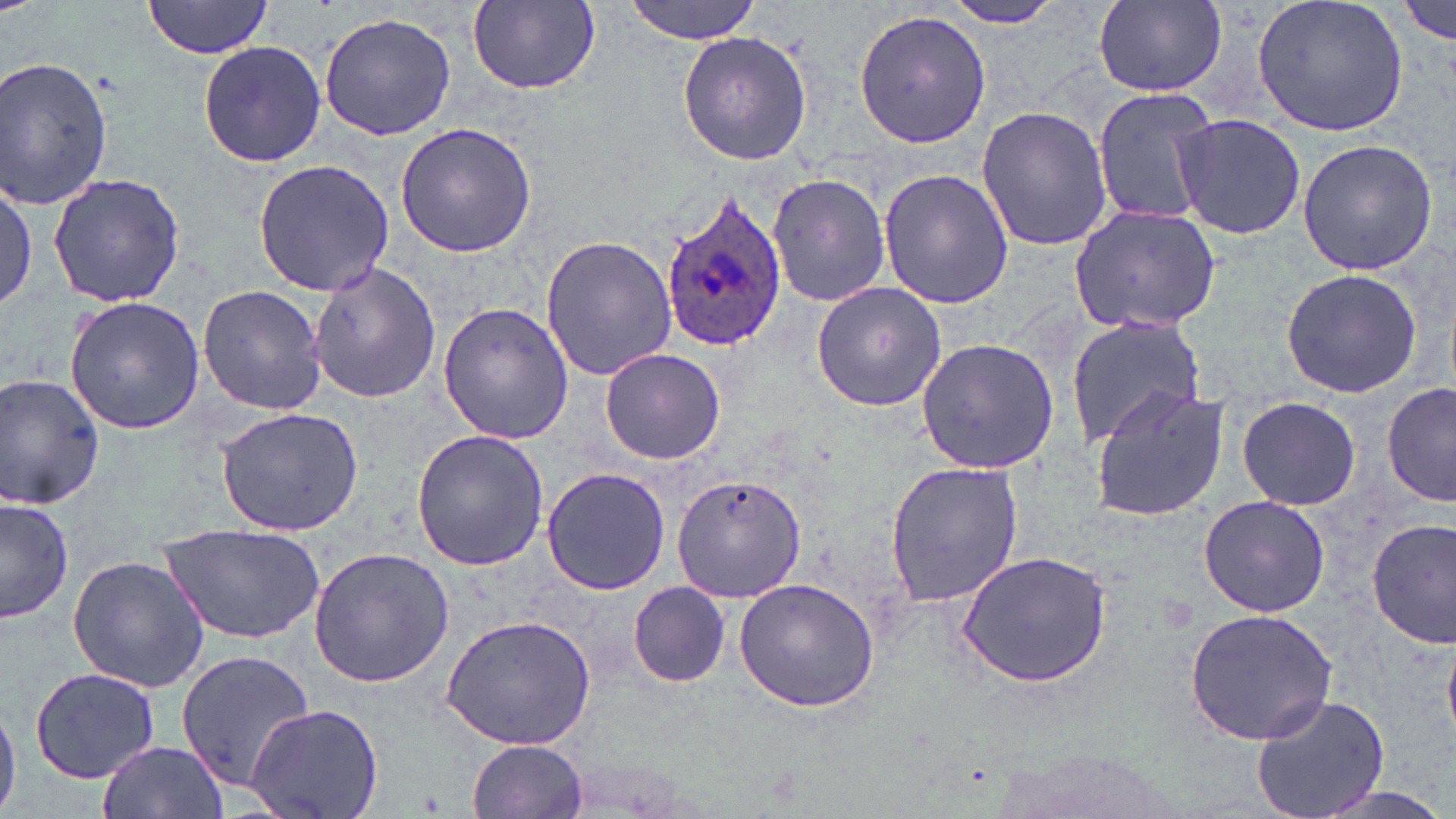

Summary:
  - Coordinate format: approximate bounding boxes as (x1,y1)-(x2,y2) corner pairs in pixels
  - Uninfected red blood cell locations: (144,0)-(272,59), (468,0)-(600,94), (623,0)-(766,43), (1250,0)-(1410,138), (1398,0)-(1454,47), (938,1)-(1072,29), (1093,2)-(1226,96), (852,9)-(993,148), (319,11)-(456,140), (677,30)-(812,166), (196,40)-(327,169), (0,56)-(114,211), (1090,87)-(1220,226), (975,106)-(1115,251), (1172,114)-(1307,241), (394,121)-(538,257), (1298,138)-(1438,276), (252,160)-(394,297), (879,168)-(1013,310), (770,171)-(888,308), (48,172)-(186,307), (0,177)-(42,317), (1068,203)-(1221,333), (541,237)-(678,380), (308,262)-(443,403), (1280,267)-(1427,398), (811,282)-(947,412), (198,285)-(329,415), (64,295)-(208,434), (437,302)-(572,445), (1064,315)-(1208,448), (915,337)-(1062,474), (599,348)-(726,463), (0,373)-(105,511), (1381,381)-(1456,508), (1089,388)-(1233,524), (1236,397)-(1363,509), (213,407)-(366,537), (412,429)-(550,571), (883,460)-(1024,607), (542,467)-(670,595), (674,475)-(805,605), (1199,495)-(1330,616), (1,497)-(75,626), (1368,518)-(1456,647), (160,523)-(325,643), (307,548)-(454,689), (955,550)-(1113,688), (66,553)-(210,693), (733,578)-(880,714), (628,581)-(731,687), (1186,608)-(1337,745), (442,614)-(598,750), (173,647)-(312,796), (29,666)-(163,785), (1249,693)-(1389,819), (0,698)-(21,818), (245,702)-(387,819), (468,738)-(589,818), (97,740)-(229,819), (1298,781)-(1456,819)
  - Plasmodium ovale-infected red blood cell locations: (655,192)-(785,351)
  - Slide-level diagnosis: Plasmodium ovale
  - Magnification: 1000x
  - Preparation: thin blood smear
  - Stain: May-Grünwald-Giemsa
  - Modality: optical microscopy
  - Image size: 1456×819 pixels
  - Field of view: one of a larger specimen